Classify this cell by malaria status.
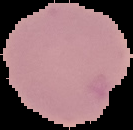

Uninfected.

Summary:
  - Preparation: thin blood film
  - Image size: 133×130 pixels
  - Image type: segmented cell region on a black background